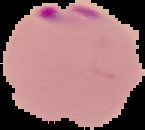
Summary:
  - Image size: 145×130 pixels
  - Result: malaria parasites detected
  - Preparation: thin blood film
  - Image type: cell region segmented out of the field of view; surrounding area masked to black